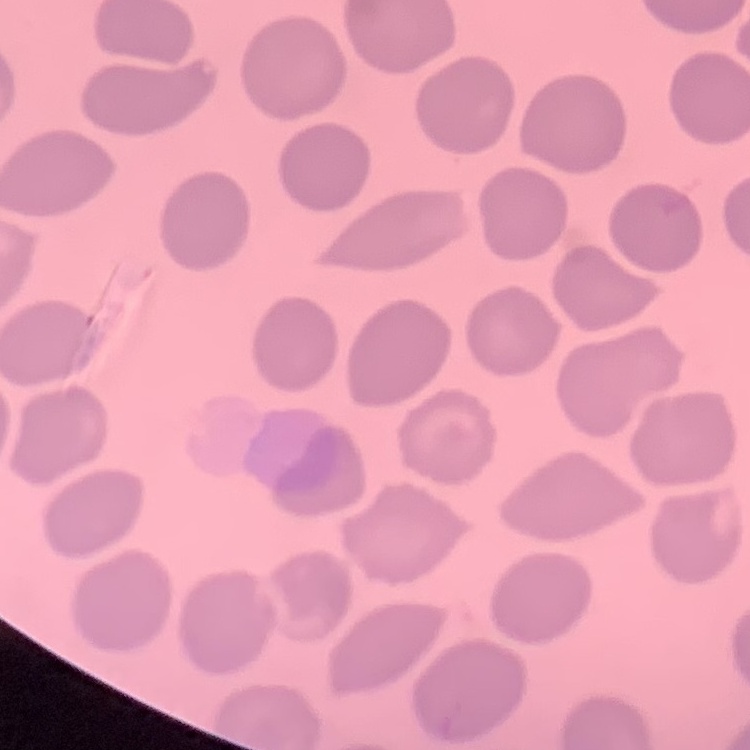

red blood cell morphology = no rouleaux formation
preparation = thin peripheral smear
image type = one tile cut from a larger photomicrograph
stain = Field's or Giemsa